Identify the preparation type.
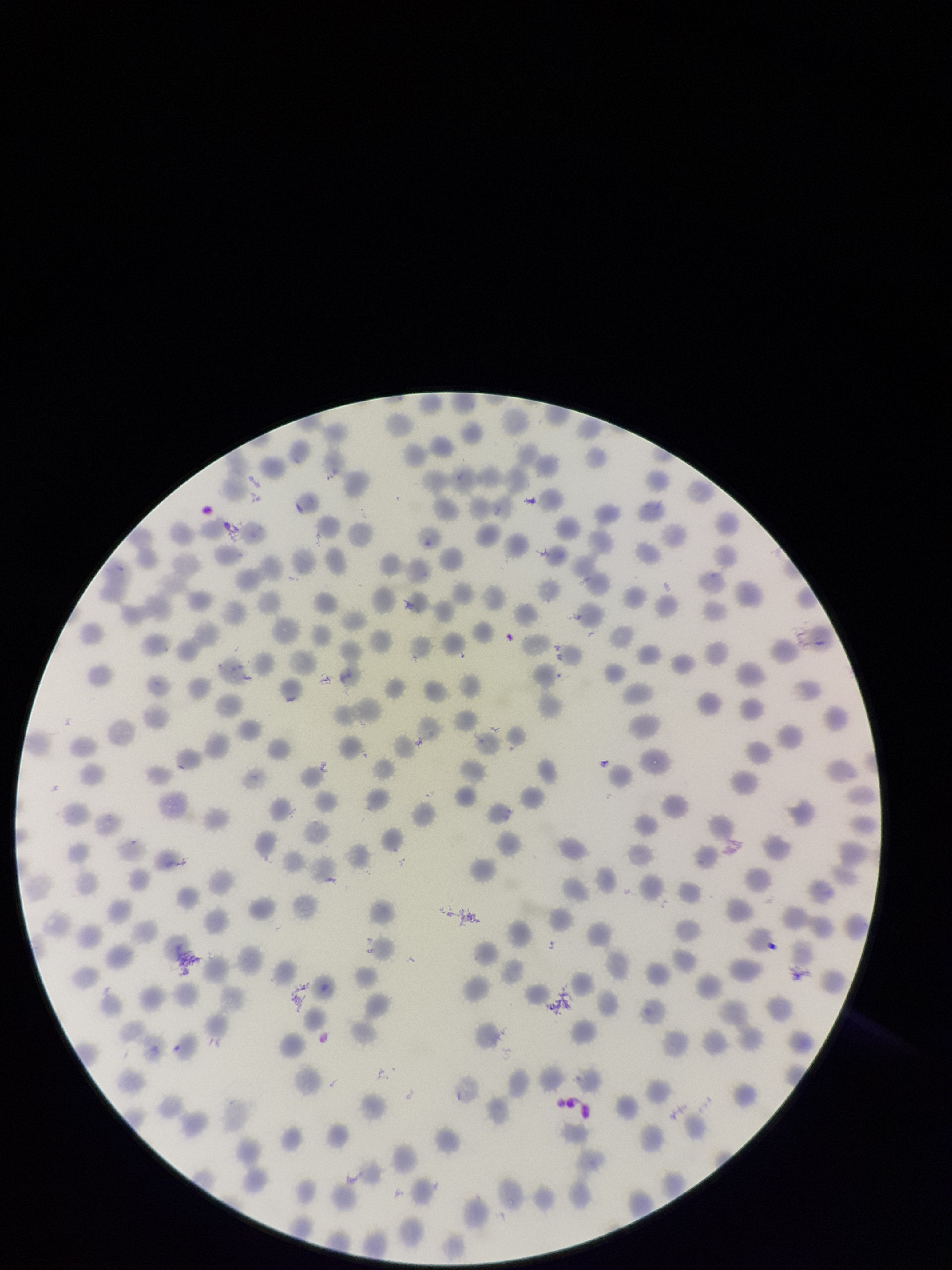
A thin smear.

field of view = single
image size = 952×1270 pixels
capture = smartphone photograph through the microscope eyepiece
red blood cell count = 256
species reported for this patient = Plasmodium falciparum
patient malaria status = positive
parasitized red blood cell count = 0
parasitized red blood cells = none detected
stain = Giemsa